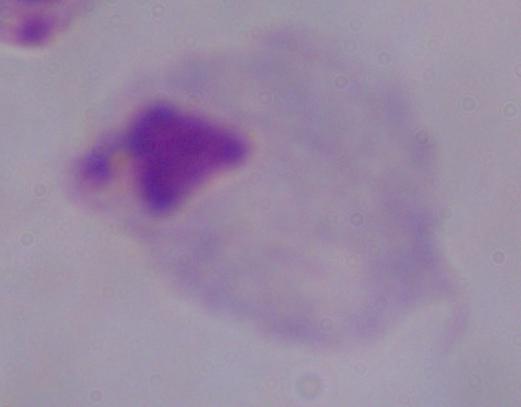
modality = micrograph
magnification = 1000x
identification = trichomonad